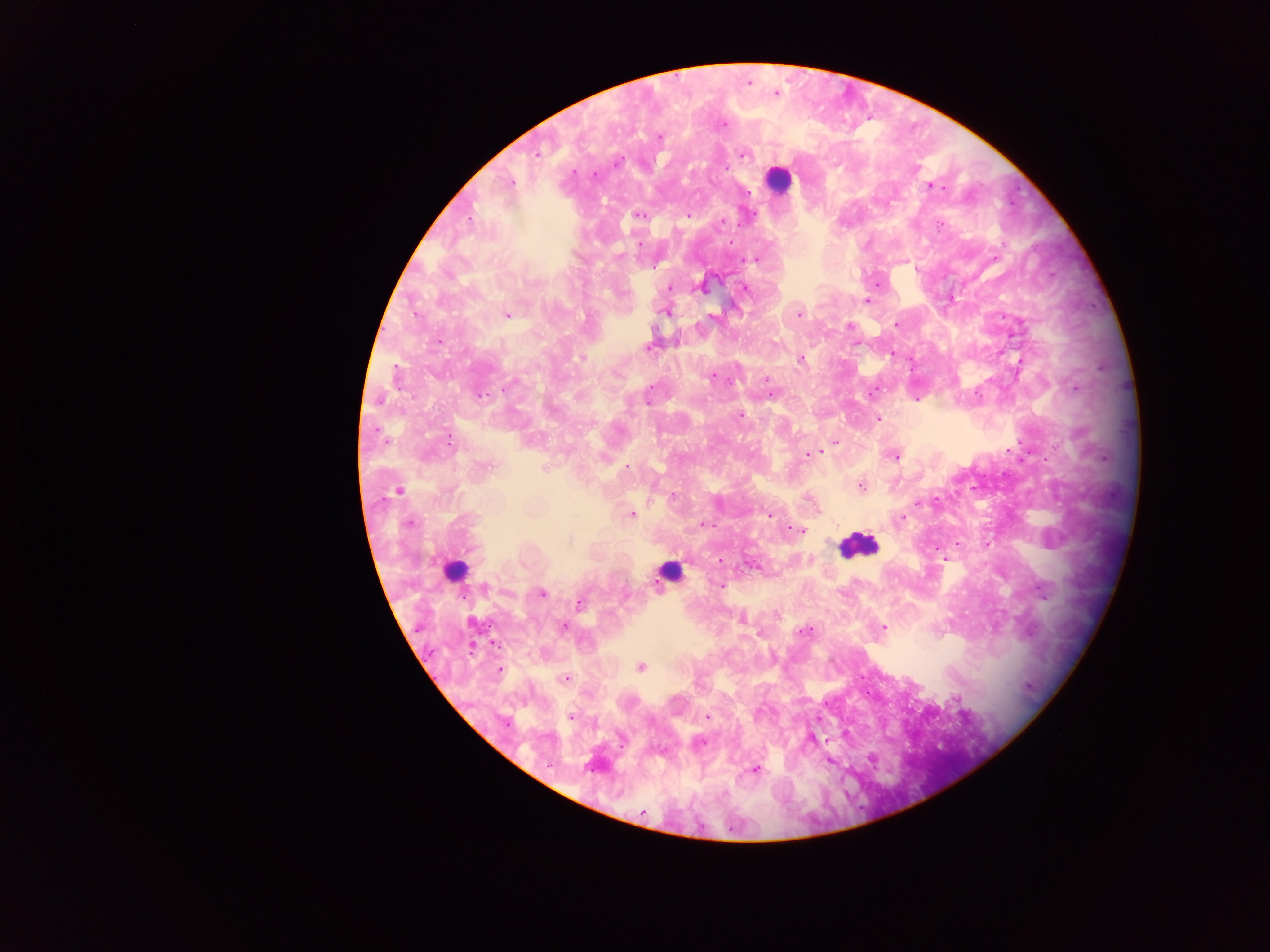

Approximate centers as x y in pixels. Leukocyte locations: 777 180; 857 545; 454 569; 667 569. Malaria parasite locations: 748 82; 774 93; 720 124; 659 138; 743 153; 534 155; 616 162; 593 174; 509 182; 931 186; 639 214; 687 216; 720 221; 758 259; 878 282; 668 287; 745 288; 867 300; 665 312; 798 312; 507 314; 896 324; 849 326; 439 341; 649 345; 581 358; 799 358; 713 376; 765 378; 478 393; 771 395; 916 399; 740 415; 878 418; 835 441; 817 453; 806 454; 894 455; 483 467; 626 468; 859 486; 399 490; 631 514; 768 515; 901 518; 409 523; 704 523; 794 530; 957 543; 945 560; 719 561; 751 563; 721 585; 541 593; 579 603; 740 619; 563 626; 883 628; 809 630; 759 633; 640 667; 499 671; 564 679; 571 717; 707 717; 811 737; 697 742; 829 760; 754 769. Single field of view. Thick blood film. Photographed through a microscope with a mobile-phone camera. Image is 1270×952 pixels. Collected in Ghana.